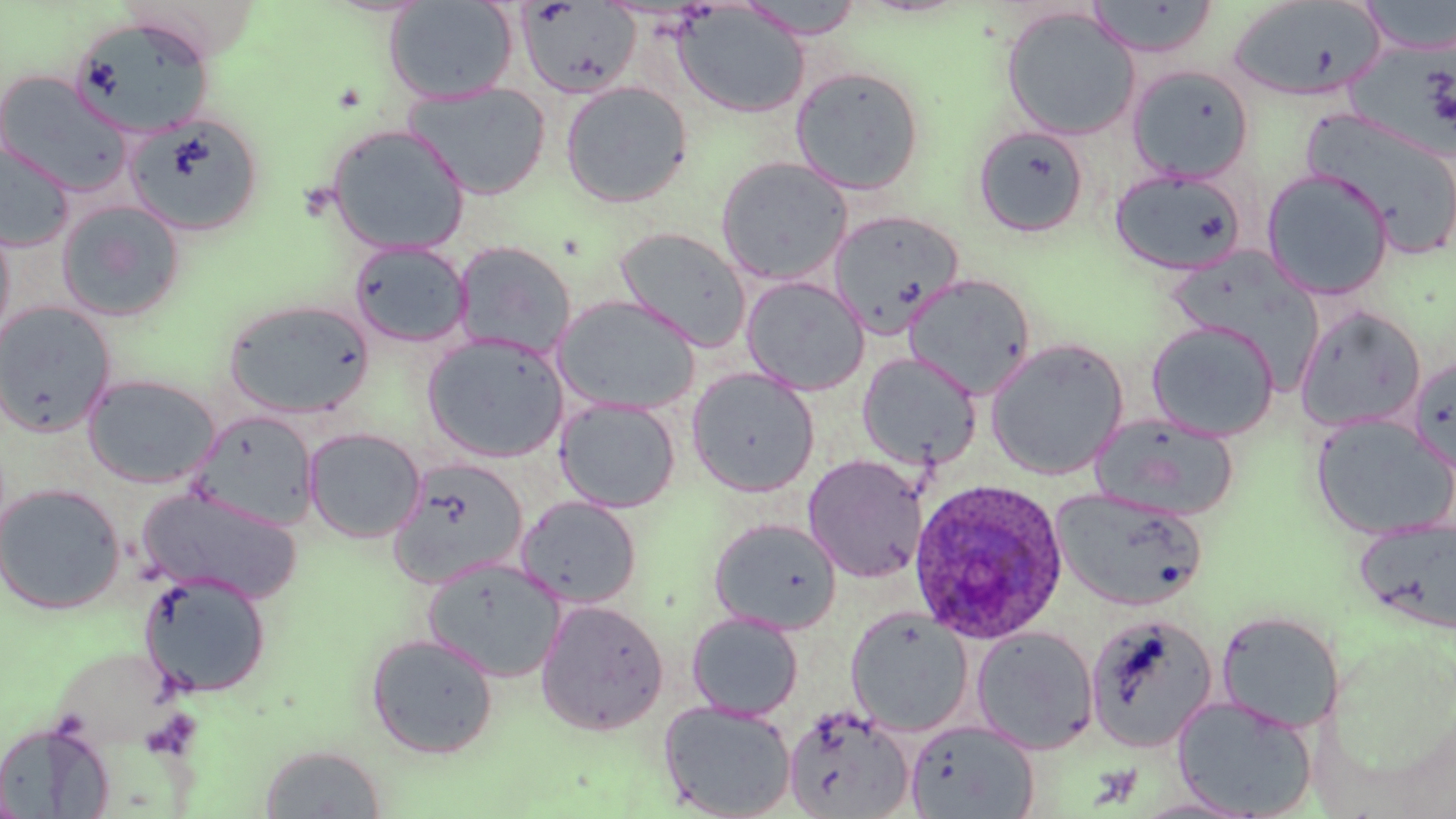

Approximate bounding boxes as [x1, y1, x2, y2] in pixels. Uninfected red blood cell locations: [735, 0, 867, 39], [1228, 0, 1387, 102], [1358, 0, 1456, 55], [383, 1, 519, 104], [516, 1, 642, 100], [1083, 1, 1219, 59], [672, 4, 809, 118], [1000, 6, 1141, 141], [69, 16, 216, 139], [1126, 63, 1255, 182], [790, 65, 925, 195], [0, 70, 133, 197], [559, 80, 693, 208], [403, 81, 551, 200], [1300, 108, 1456, 259], [122, 112, 264, 237], [973, 123, 1090, 238], [324, 124, 471, 256], [0, 143, 75, 252], [715, 156, 853, 285], [1110, 168, 1248, 276], [1261, 168, 1395, 300], [56, 199, 186, 322], [828, 210, 965, 335], [0, 216, 16, 354], [615, 226, 752, 351], [349, 240, 472, 348], [453, 241, 576, 359], [1167, 247, 1321, 375], [902, 273, 1037, 398], [740, 275, 870, 395], [552, 294, 701, 415], [223, 298, 374, 419], [0, 301, 116, 437], [1294, 305, 1427, 432], [1147, 320, 1279, 441], [422, 332, 570, 463], [985, 337, 1129, 480], [857, 351, 982, 471], [1407, 354, 1456, 472], [686, 367, 820, 496], [82, 373, 221, 488], [555, 397, 681, 512], [191, 411, 319, 528], [1091, 411, 1239, 520], [1311, 413, 1456, 539], [303, 427, 426, 543], [803, 454, 928, 583], [388, 457, 529, 587], [0, 483, 125, 614], [137, 487, 301, 602], [1051, 487, 1207, 612], [515, 495, 642, 609], [1354, 516, 1456, 635], [708, 517, 842, 635], [421, 557, 565, 682], [138, 570, 272, 698], [534, 598, 669, 737], [845, 607, 974, 736], [1216, 610, 1345, 733], [686, 612, 804, 721], [1084, 614, 1218, 752], [970, 626, 1099, 754], [364, 632, 499, 758], [1172, 695, 1317, 818], [658, 700, 796, 819], [782, 704, 915, 819], [905, 720, 1040, 819], [1, 727, 115, 819], [258, 743, 388, 818]. Plasmodium ovale-infected red blood cell locations: [908, 478, 1069, 644]. Slide-level diagnosis: Plasmodium ovale. Single field of view. Captured at 1000x magnification. May-Grünwald-Giemsa-stained preparation. Light microscopy. Thin blood smear. Image is 1456×819 pixels.